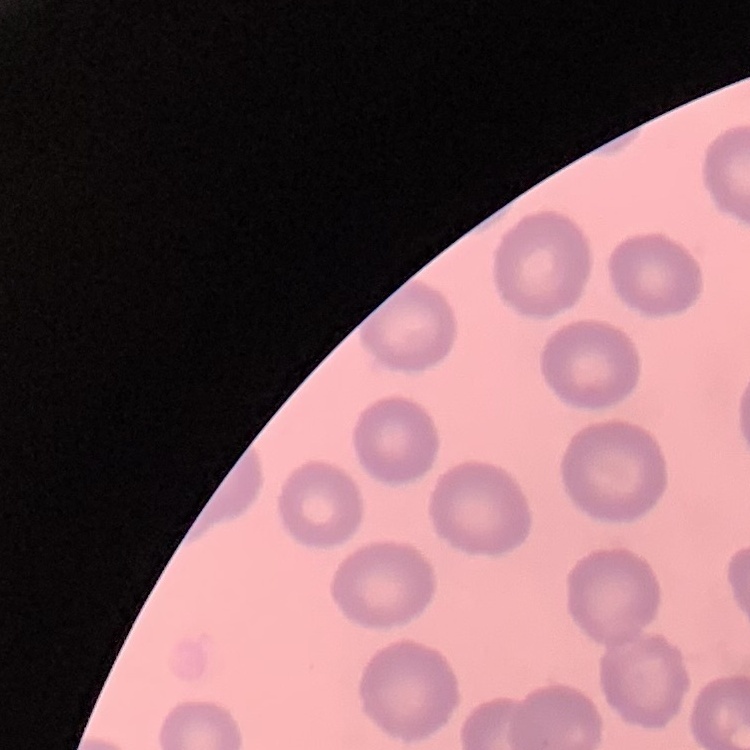

The red blood cells exhibit no rouleaux formation. One tile cut from a larger photomicrograph. Thin blood smear. Field's or Giemsa stain.